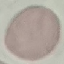

malaria_status: uninfected
preparation: thin blood film
image_type: automatically extracted cell patch, resized to 64 × 64 pixels
stain: Giemsa
capture: smartphone through the microscope eyepiece